Assess this cell for malaria.
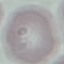
It is uninfected.

Thin blood film. Acquired by smartphone through the microscope eyepiece. Cell patch, automatically extracted from a larger field of view and resized to 64 × 64 pixels. Giemsa stain.